State which parasite is depicted.
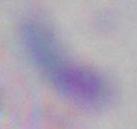
This is Toxoplasma gondii.

magnification = 1000x
modality = micrograph